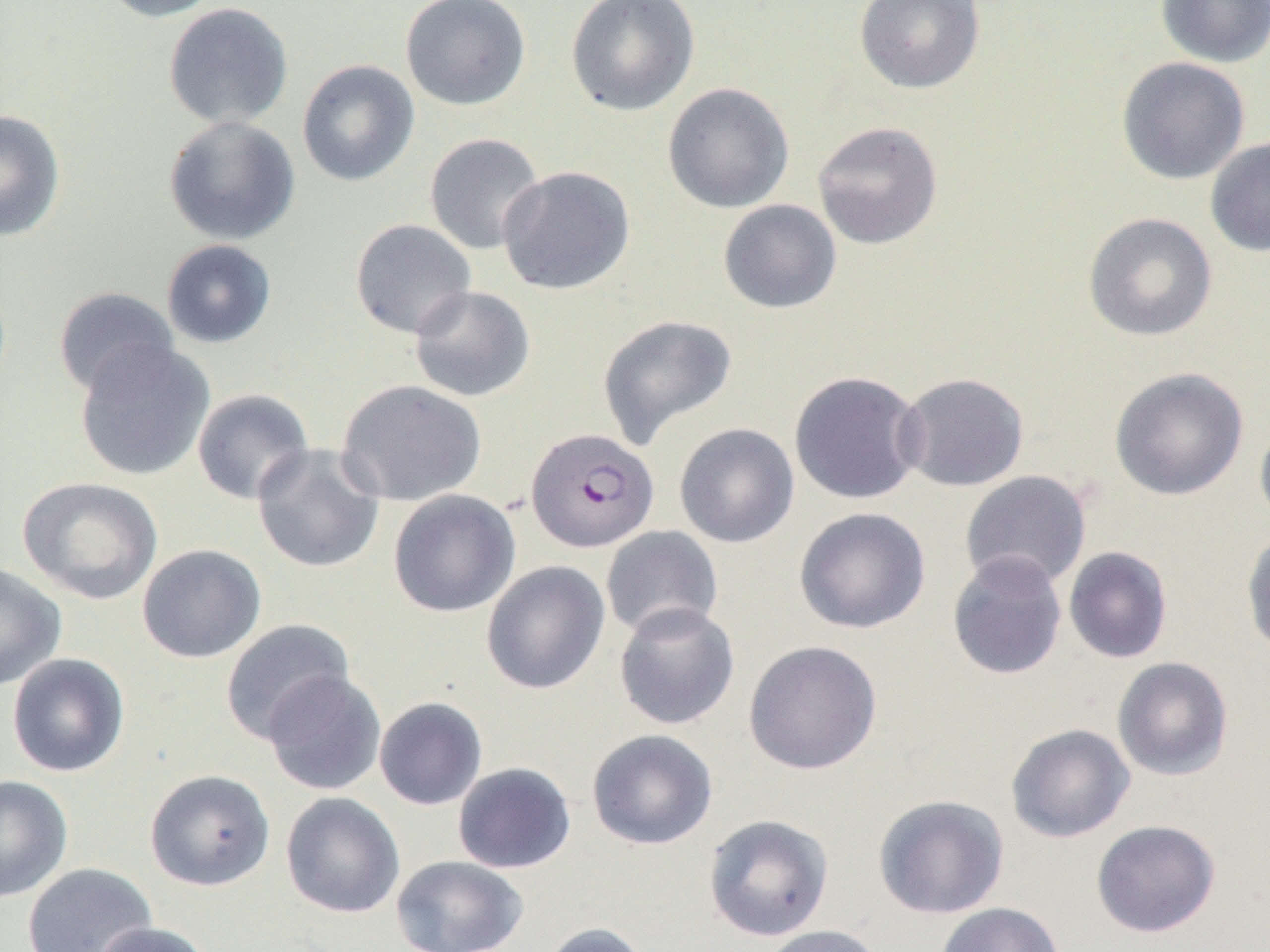

slide-level diagnosis = Plasmodium falciparum
preparation = thin blood film
modality = optical microscopy
image size = 1270×952 pixels
Plasmodium falciparum-infected red blood cell locations = approximate bounding boxes as (x1,y1)-(x2,y2) corner pairs in pixels: (525,428)-(659,554)
uninfected red blood cell locations = approximate bounding boxes as (x1,y1)-(x2,y2) corner pairs in pixels: (98,0)-(226,22), (400,0)-(532,110), (566,0)-(700,116), (854,0)-(986,94), (1155,0)-(1270,68), (162,1)-(294,130), (1116,56)-(1250,185), (297,59)-(420,187), (662,82)-(795,213), (0,109)-(66,241), (163,115)-(300,246), (812,121)-(944,250), (424,132)-(546,255), (1205,136)-(1270,257), (498,166)-(635,295), (718,199)-(842,314), (1082,212)-(1218,342), (349,219)-(477,340), (161,239)-(277,348), (409,285)-(536,402), (54,286)-(179,398), (596,314)-(738,449), (74,341)-(215,481), (1109,367)-(1249,500), (788,370)-(926,505), (895,372)-(1030,492), (336,378)-(487,506), (192,389)-(314,505), (1254,416)-(1270,532), (674,423)-(799,548), (251,444)-(385,573), (960,470)-(1092,590), (16,476)-(163,605), (388,489)-(520,618), (794,507)-(930,634), (600,526)-(723,639), (1241,528)-(1270,661), (137,544)-(266,663), (1063,546)-(1173,663), (947,551)-(1067,680), (481,560)-(610,695), (0,563)-(67,690), (613,601)-(740,730), (219,618)-(355,744), (744,640)-(882,775), (6,653)-(130,777), (1111,656)-(1234,781), (262,671)-(387,795), (373,696)-(488,810), (1005,723)-(1136,843), (586,728)-(718,850), (452,762)-(576,873), (144,769)-(275,891), (0,775)-(73,902), (280,792)-(405,919), (873,794)-(1009,919), (703,814)-(834,941), (1091,819)-(1221,938), (390,855)-(529,952), (22,862)-(157,952), (936,902)-(1065,952), (93,921)-(214,952), (538,921)-(651,952), (757,925)-(886,952)
magnification = 1000x
field of view = one of a larger specimen